Assess this cell for malaria.
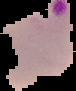
It is parasitized.

Summary:
  - Image type: segmented cell region on a black background
  - Preparation: thin blood smear
  - Image size: 76×91 pixels